Report the malaria status of this cell.
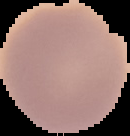
Uninfected.

Summary:
  - Image size: 130×136 pixels
  - Preparation: thin blood film
  - Image type: cell region segmented out of the field of view; surrounding area masked to black